Classify this cell by malaria status.
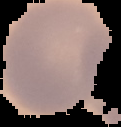
Uninfected.

Segmented cell region on a black background. Image is 121×127 pixels. From a thin blood film.